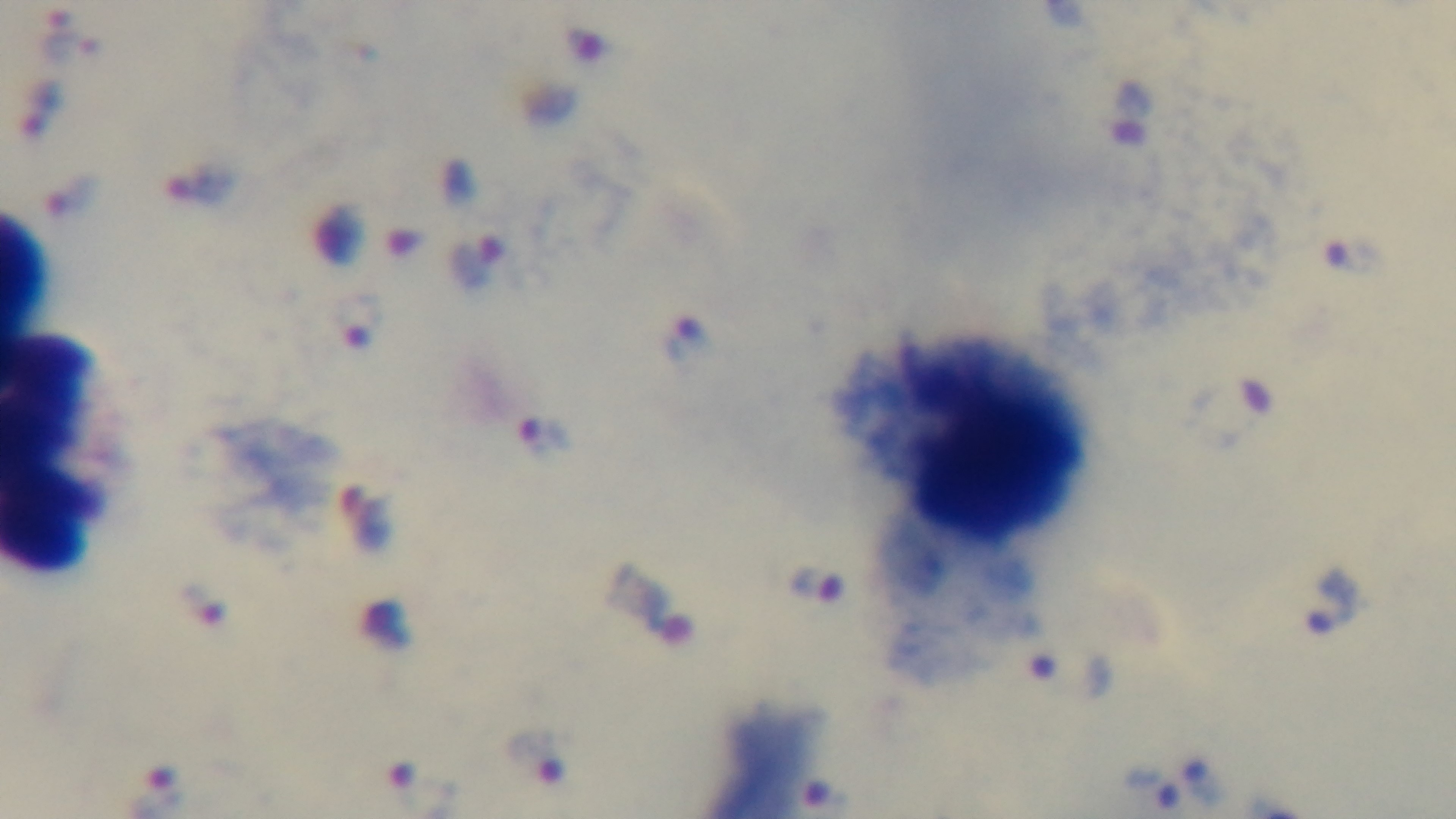
Malaria status: positive. Preparation: thick blood film. Captured with a mounted 4K digital camera. Oil-immersion objective, 100x. One field from the slide. Giemsa stain. Light microscopy.